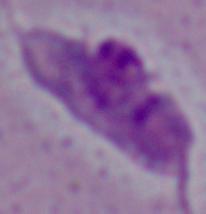

Summary:
  - Magnification: 1000x
  - Modality: photomicrograph
  - Identification: Leishmania